Describe the morphology of the red blood cells.
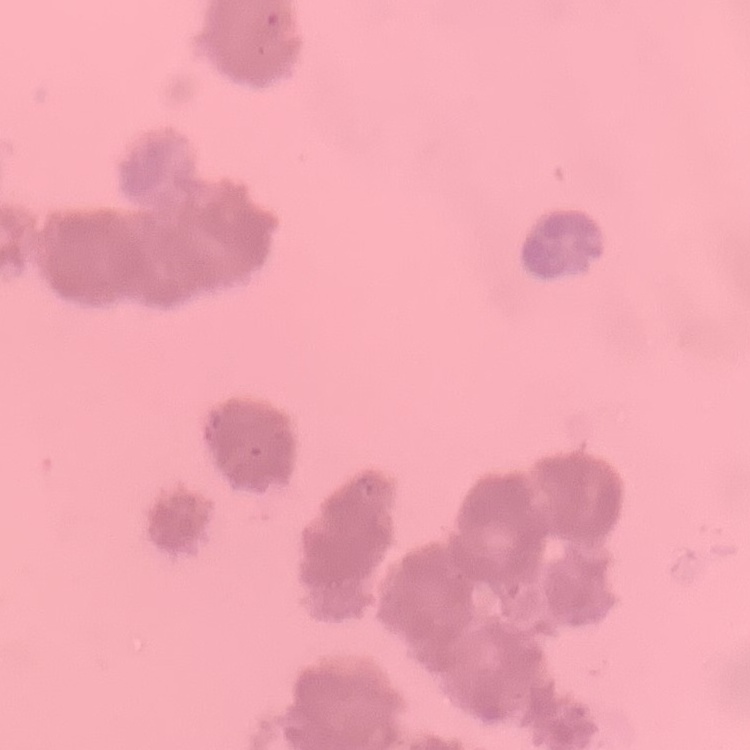
They show rouleaux formation.

Square crop of a larger photomicrograph. Stained with either Field's or Giemsa. Thin blood film.